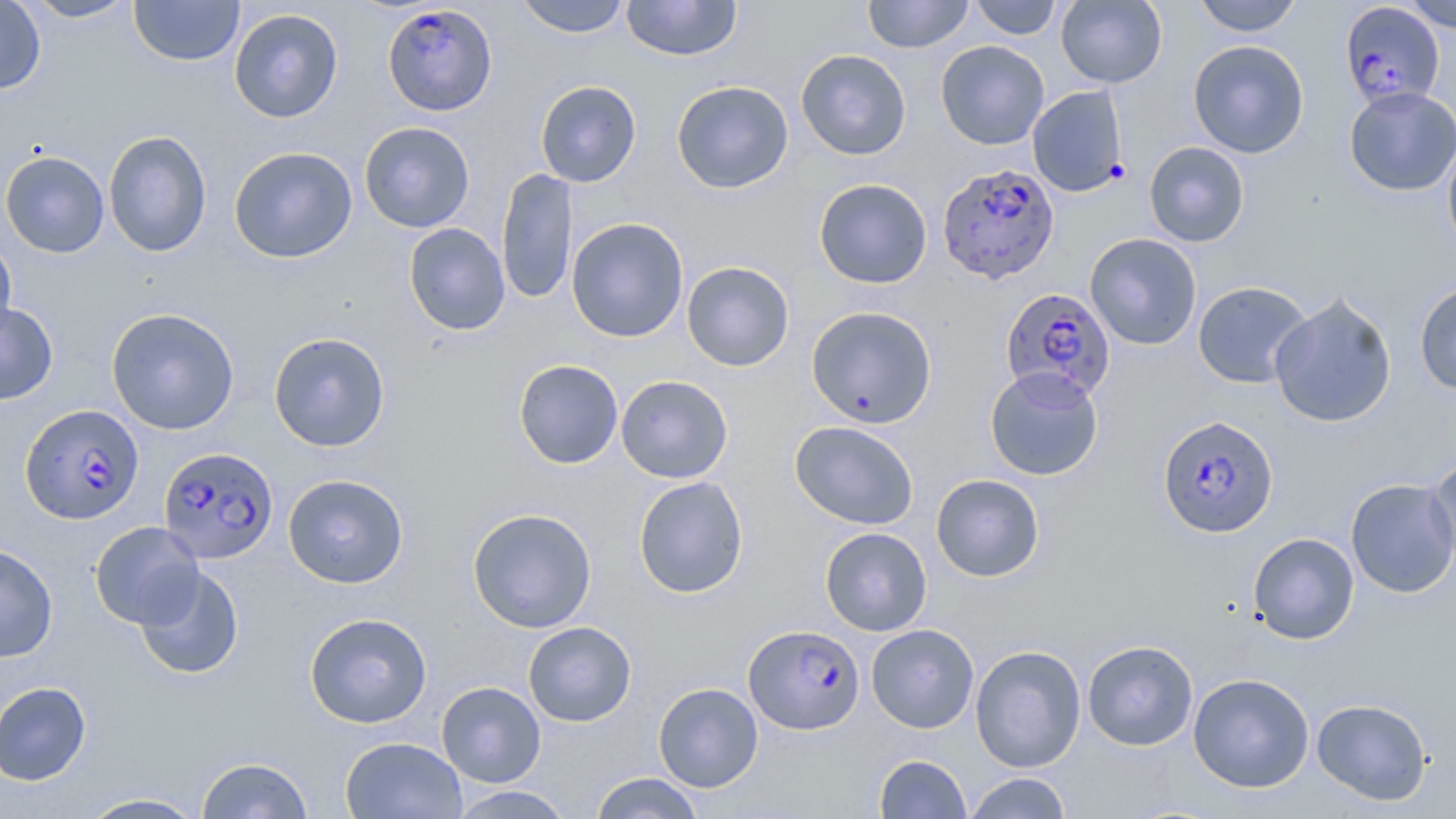
Summary:
  - Coordinate format: approximate bounding boxes as (x1,y1)-(x2,y2) corner pairs in pixels
  - Uninfected red blood cell locations: (0,0)-(47,95), (20,0)-(139,22), (128,0)-(245,66), (515,0)-(631,38), (622,0)-(742,61), (864,0)-(973,53), (969,0)-(1062,40), (1056,0)-(1167,88), (1192,0)-(1304,37), (1400,1)-(1456,32), (228,8)-(344,123), (935,40)-(1050,150), (1188,40)-(1309,158), (796,49)-(911,160), (535,80)-(641,187), (671,80)-(794,193), (1027,86)-(1129,197), (1344,86)-(1456,196), (359,121)-(475,233), (102,130)-(212,257), (1442,135)-(1456,258), (1145,142)-(1251,247), (228,146)-(358,264), (0,150)-(110,258), (496,167)-(577,306), (814,178)-(932,289), (566,217)-(689,343), (403,223)-(510,336), (1084,233)-(1202,350), (0,237)-(17,345), (681,261)-(795,371), (1192,281)-(1313,388), (1414,281)-(1456,395), (1269,291)-(1398,428), (0,301)-(58,405), (806,305)-(937,429), (106,307)-(240,435), (268,332)-(390,452), (513,359)-(623,469), (985,366)-(1104,481), (616,375)-(733,483), (790,420)-(919,530), (1426,452)-(1456,574), (283,473)-(409,589), (930,473)-(1045,581), (633,476)-(749,598), (1345,478)-(1456,598), (467,508)-(597,633), (90,521)-(204,628), (819,527)-(932,636), (1248,533)-(1359,644), (0,543)-(58,663), (133,565)-(244,680), (304,612)-(433,728), (523,621)-(636,727), (866,624)-(979,733), (1082,639)-(1198,751), (970,645)-(1087,772), (1188,672)-(1314,793), (0,681)-(92,785), (436,681)-(546,787), (653,682)-(764,792), (1312,697)-(1432,805), (339,736)-(467,819), (874,754)-(972,818), (195,756)-(314,818), (589,772)-(706,819), (964,772)-(1073,819), (448,786)-(575,818), (77,792)-(209,818)
  - Plasmodium falciparum-infected red blood cell locations: (382,4)-(497,117), (1347,6)-(1444,121), (937,163)-(1059,284), (1000,288)-(1116,403), (21,405)-(142,522), (1157,415)-(1279,538), (158,446)-(278,563), (742,624)-(864,735)
  - Slide-level diagnosis: Plasmodium falciparum
  - Preparation: thin blood smear
  - Field of view: single
  - Magnification: 1000x
  - Modality: light microscopy
  - Stain: May-Grünwald-Giemsa
  - Image size: 1456×819 pixels